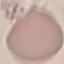

Summary:
  - Result: no malaria parasites seen
  - Capture: smartphone camera at the microscope eyepiece
  - Preparation: thin blood smear
  - Image type: automatically extracted cell patch, resized to 64 × 64 pixels
  - Stain: Giemsa